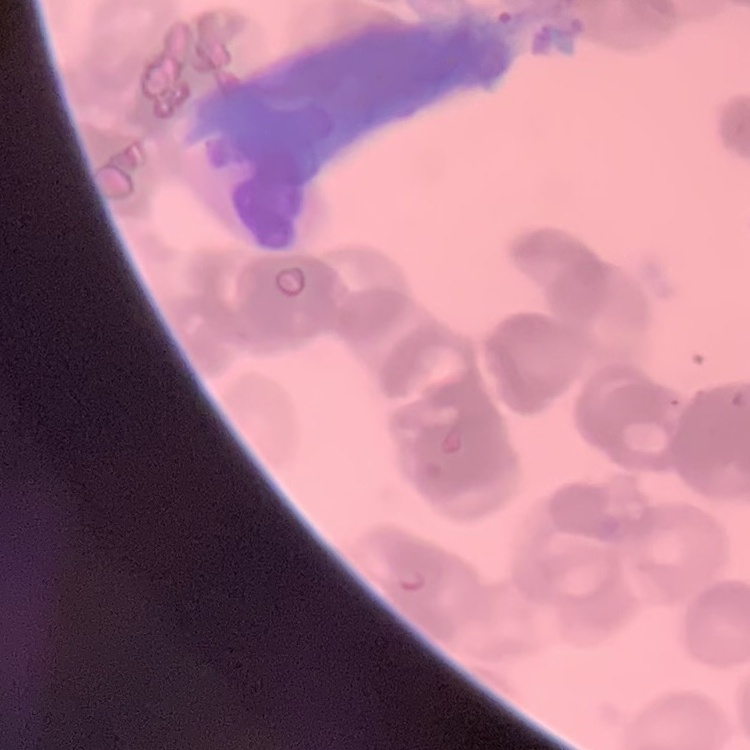

{
  "red_blood_cell_morphology": "rouleaux formation",
  "stain": "Field's or Giemsa",
  "preparation": "thin blood film",
  "image_type": "square crop of a larger photomicrograph"
}